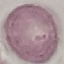

result = no malaria parasites detected
capture = smartphone camera at the microscope eyepiece
image type = cell patch, automatically extracted from a larger field of view and resized to 64 × 64 pixels
preparation = thin blood smear
stain = Giemsa